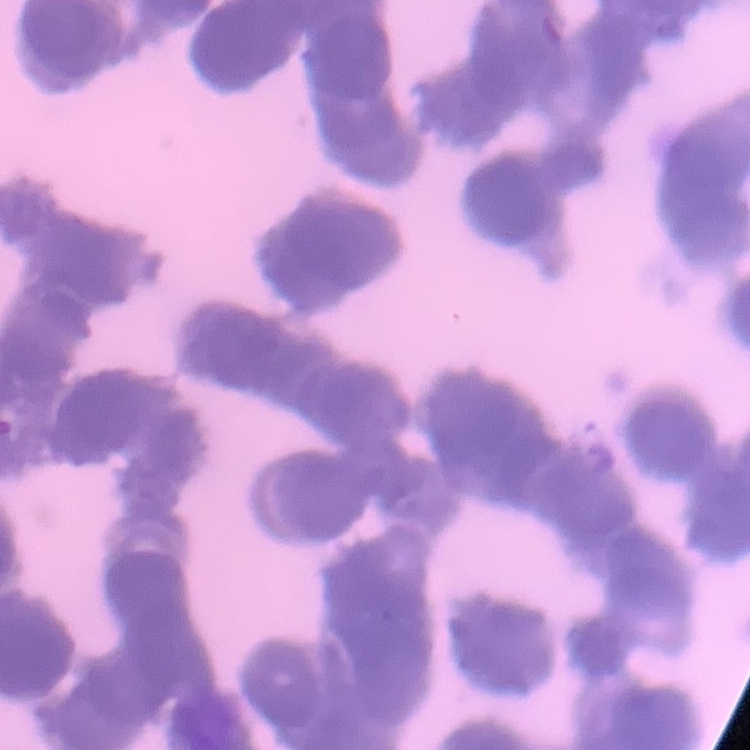
Summary:
  - Red blood cell morphology: rouleaux formation
  - Preparation: thin blood smear
  - Stain: Field's or Giemsa
  - Image type: square crop of a larger photomicrograph